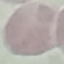

Malaria status: uninfected. Acquired by smartphone through the microscope eyepiece. Cell patch, automatically extracted from a larger field of view and resized to 64 × 64 pixels. Giemsa stain. Thin blood film.